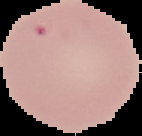
{
  "result": "negative for Plasmodium parasites",
  "preparation": "thin blood smear",
  "image_type": "cell region segmented out of the field of view; surrounding area masked to black",
  "image_size": "142×136 pixels"
}